Comment on the morphology of the erythrocytes.
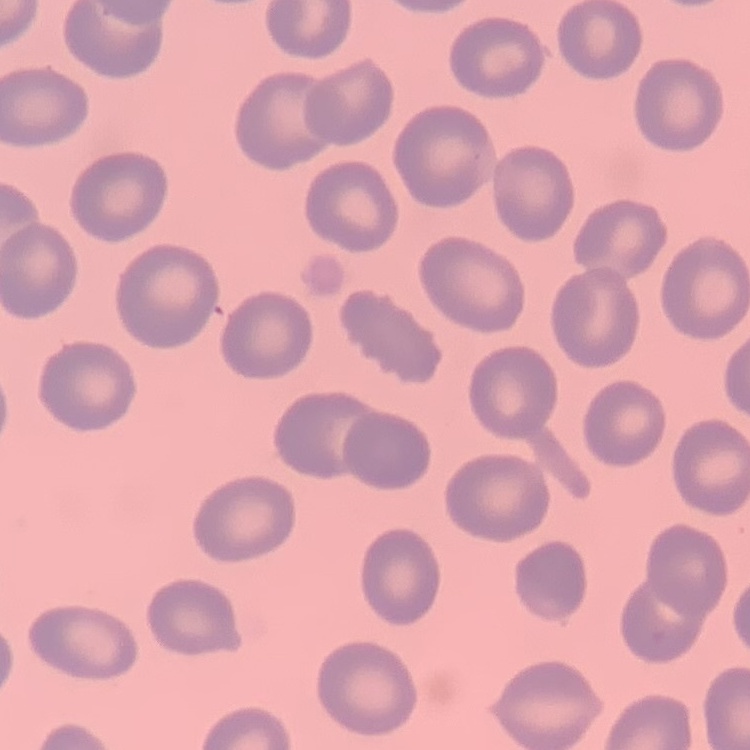
No rouleaux formation.

Thin blood film. Stained with either Field's or Giemsa. One tile cut from a larger photomicrograph.